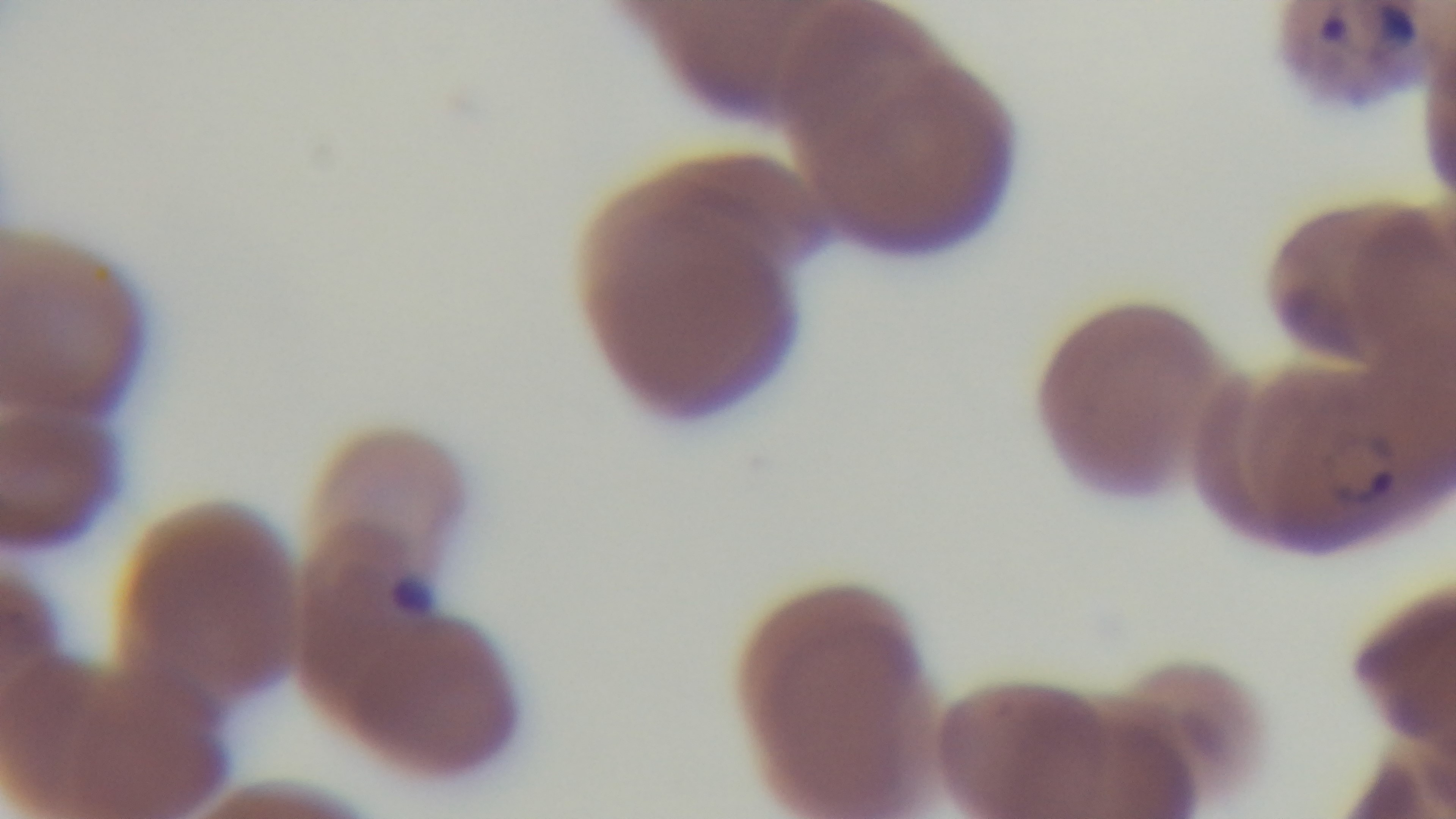

modality: light microscopy
stain: Giemsa
field_of_view: single
capture: mounted 4K digital camera
malaria_status: infected
objective: 100x oil immersion
preparation: thin